Assess this cell for malaria.
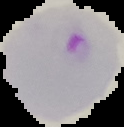

It is parasitized.

From a thin blood film. The area outside the segmented cell region is set to black. Image is 124×127 pixels.